Locate every blood parasite and identify its species.
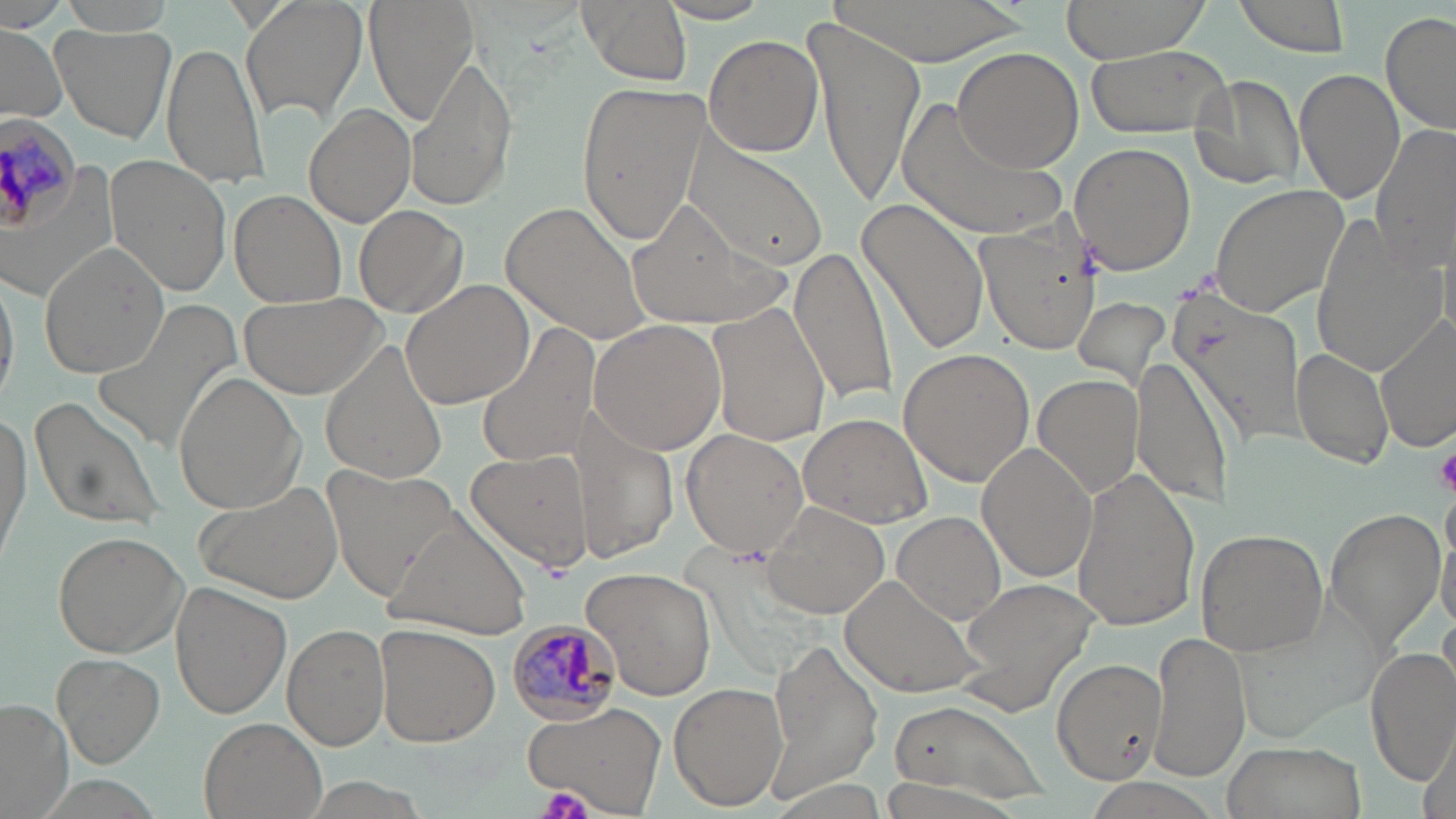

Approximate bounding boxes as (x1,y1)-(x2,y2) corner pairs in pixels.
Plasmodium malariae-infected red blood cells: (0,117)-(82,235), (505,620)-(619,726).
No Plasmodium falciparum, Plasmodium ovale, Plasmodium vivax, Babesia divergens, or Trypanosoma brucei observed.

Summary:
  - Platelet locations: (1435,445)-(1456,495), (541,785)-(593,819)
  - Uninfected red blood cell locations: (56,0)-(181,35), (241,0)-(368,126), (367,0)-(476,124), (574,0)-(694,86), (836,0)-(1026,61), (1057,0)-(1211,67), (1231,0)-(1352,57), (652,2)-(773,25), (1378,11)-(1456,136), (810,17)-(923,207), (0,22)-(67,120), (52,22)-(178,143), (703,34)-(824,157), (161,38)-(268,189), (1085,43)-(1235,139), (953,47)-(1084,174), (409,55)-(518,213), (1295,68)-(1407,207), (1189,72)-(1308,192), (574,80)-(708,247), (895,99)-(1067,245), (303,104)-(416,227), (1372,123)-(1456,272), (680,134)-(829,272), (1069,142)-(1198,274), (107,156)-(231,295), (1210,182)-(1353,319), (230,190)-(346,308), (856,197)-(991,357), (628,200)-(784,335), (505,202)-(650,343), (354,204)-(469,319), (1309,214)-(1446,376), (977,217)-(1102,358), (37,241)-(172,378), (787,244)-(900,406), (0,267)-(17,408), (398,280)-(533,410), (1172,290)-(1309,446), (241,291)-(385,398), (1070,295)-(1173,397), (92,296)-(247,454), (707,304)-(830,445), (1374,317)-(1455,451), (586,318)-(729,455), (474,323)-(600,471), (319,339)-(451,488), (897,348)-(1035,488), (1292,348)-(1395,472), (1133,355)-(1235,508), (173,371)-(306,513), (1032,374)-(1141,500), (28,394)-(165,530), (0,409)-(32,563), (798,413)-(932,529), (577,414)-(678,563), (680,430)-(808,558), (976,443)-(1098,583), (466,447)-(591,572), (324,466)-(461,593), (1069,469)-(1202,630), (193,479)-(346,602), (762,501)-(890,620), (1324,505)-(1446,654), (893,512)-(1007,623), (391,518)-(533,637), (1437,524)-(1456,634), (1195,528)-(1329,655), (52,530)-(187,657), (584,566)-(716,701), (842,575)-(986,698), (953,579)-(1102,715), (172,581)-(289,719), (283,622)-(390,750), (376,624)-(500,746), (1148,629)-(1248,783), (767,638)-(883,795), (1367,644)-(1455,790), (52,653)-(164,768), (1052,657)-(1164,783), (669,680)-(788,810), (0,700)-(74,819), (523,701)-(667,817), (887,705)-(1031,797), (198,717)-(328,819), (1421,726)-(1455,819), (1222,738)-(1367,819)
  - Slide-level diagnosis: Plasmodium malariae
  - Magnification: 1000x
  - Stain: May-Grünwald-Giemsa
  - Preparation: thin blood smear
  - Image size: 1456×819 pixels
  - Field of view: one of a larger specimen
  - Modality: optical microscopy